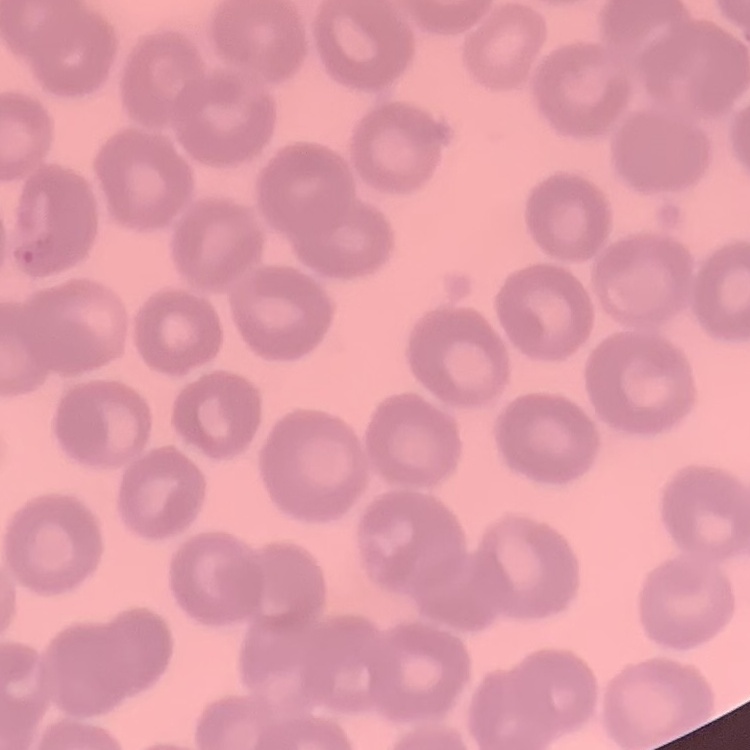

The red blood cells exhibit no rouleaux formation. Stained with either Field's or Giemsa. Thin peripheral smear. Square crop of a larger photomicrograph.